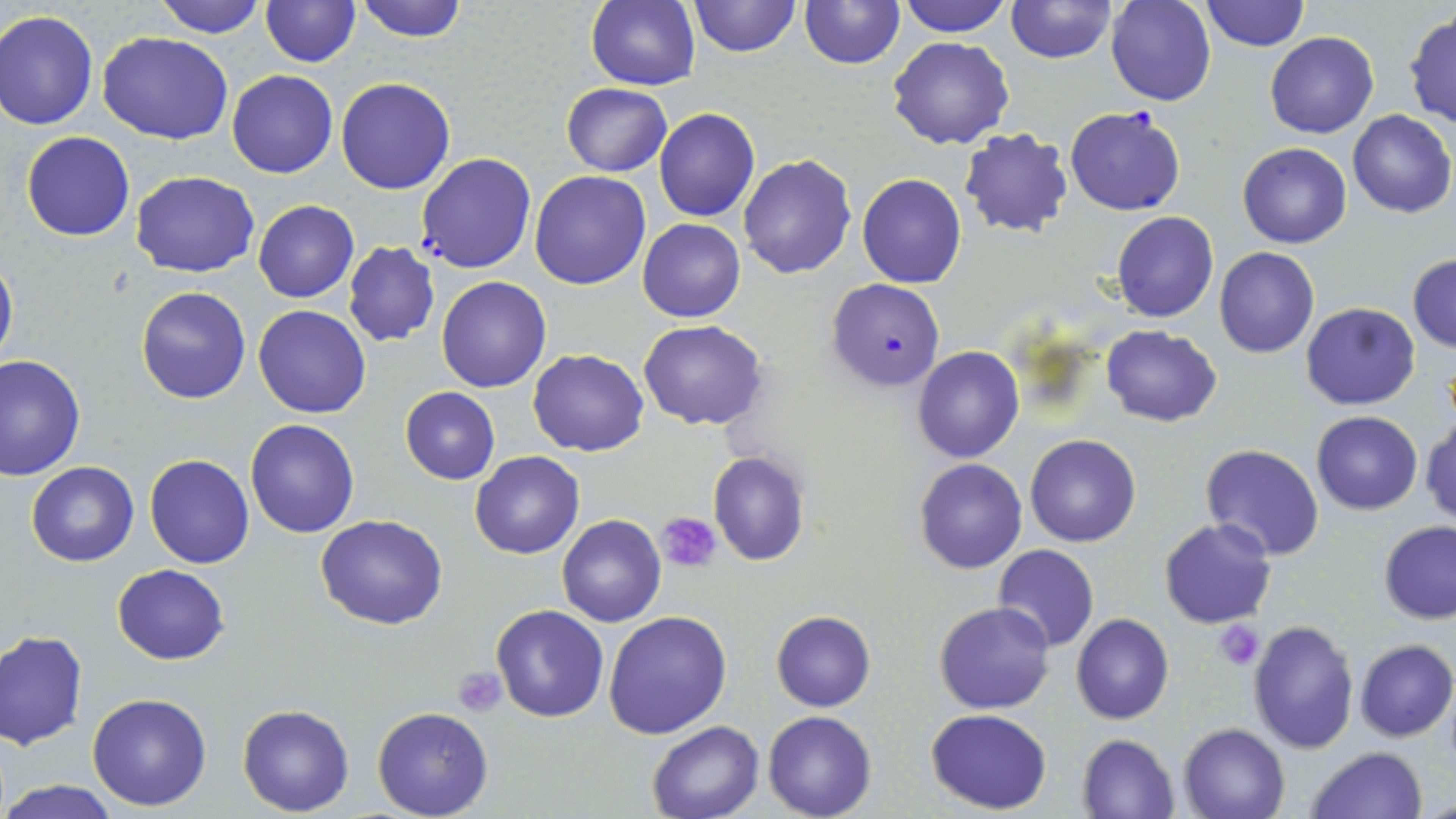

Summary:
  - Coordinate format: approximate bounding boxes as (x1, y1, x2, y2) in pixels
  - Uninfected red blood cell locations: (153, 0, 267, 37), (261, 0, 359, 67), (354, 0, 468, 43), (687, 0, 801, 56), (896, 0, 1013, 37), (1006, 0, 1117, 65), (1106, 0, 1216, 107), (1199, 0, 1310, 51), (586, 1, 699, 90), (799, 1, 905, 69), (0, 9, 99, 130), (1404, 9, 1456, 131), (97, 31, 233, 144), (1266, 32, 1379, 138), (886, 37, 1015, 150), (228, 70, 338, 178), (336, 77, 456, 195), (560, 83, 672, 176), (1064, 104, 1187, 216), (654, 108, 760, 222), (1347, 110, 1454, 218), (958, 128, 1072, 238), (21, 130, 136, 241), (1237, 142, 1352, 247), (738, 154, 856, 280), (130, 171, 258, 275), (530, 171, 651, 291), (858, 173, 967, 288), (253, 200, 359, 302), (1112, 211, 1218, 322), (639, 218, 746, 321), (342, 241, 441, 348), (1215, 247, 1320, 359), (0, 254, 17, 375), (1407, 254, 1455, 352), (435, 276, 552, 393), (135, 285, 252, 403), (138, 294, 370, 410), (1301, 302, 1420, 411), (253, 304, 372, 419), (639, 320, 767, 430), (1100, 325, 1222, 426), (913, 347, 1024, 463), (528, 348, 649, 456), (0, 355, 84, 478), (400, 388, 500, 485), (1311, 410, 1423, 515), (1421, 415, 1456, 526), (245, 418, 359, 538), (1025, 433, 1142, 548), (1200, 444, 1325, 562), (469, 450, 585, 559), (708, 450, 811, 566), (144, 453, 255, 569), (915, 458, 1027, 574), (26, 462, 139, 566), (315, 513, 448, 630), (557, 513, 666, 628), (1159, 518, 1277, 629), (1379, 520, 1456, 623), (993, 545, 1099, 652), (114, 564, 229, 664), (935, 601, 1054, 714), (491, 605, 609, 723), (603, 610, 732, 739), (771, 610, 875, 711), (1072, 614, 1174, 725), (1247, 619, 1360, 755), (0, 631, 87, 751), (1354, 639, 1455, 741), (87, 692, 213, 811), (237, 704, 354, 815), (371, 707, 493, 819), (926, 709, 1053, 814), (763, 711, 878, 819), (646, 720, 766, 819), (1179, 722, 1291, 819), (1078, 734, 1180, 819), (1307, 746, 1427, 819), (0, 779, 123, 817), (1423, 793, 1456, 818)
  - Platelet locations: (658, 512, 721, 572), (1214, 623, 1264, 670), (453, 666, 507, 717)
  - Plasmodium falciparum-infected red blood cell locations: (958, 120, 1184, 228), (417, 153, 536, 274), (827, 279, 944, 389)
  - Slide-level diagnosis: Plasmodium falciparum
  - Modality: light microscopy
  - Preparation: thin blood film
  - Field of view: single
  - Stain: May-Grünwald-Giemsa
  - Image size: 1456×819 pixels
  - Magnification: 1000x